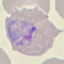 Result: malaria parasites detected. Acquired by smartphone through the microscope eyepiece. Thin blood film. Giemsa-stained preparation. Automatically extracted cell patch, resized to 64 × 64 pixels.